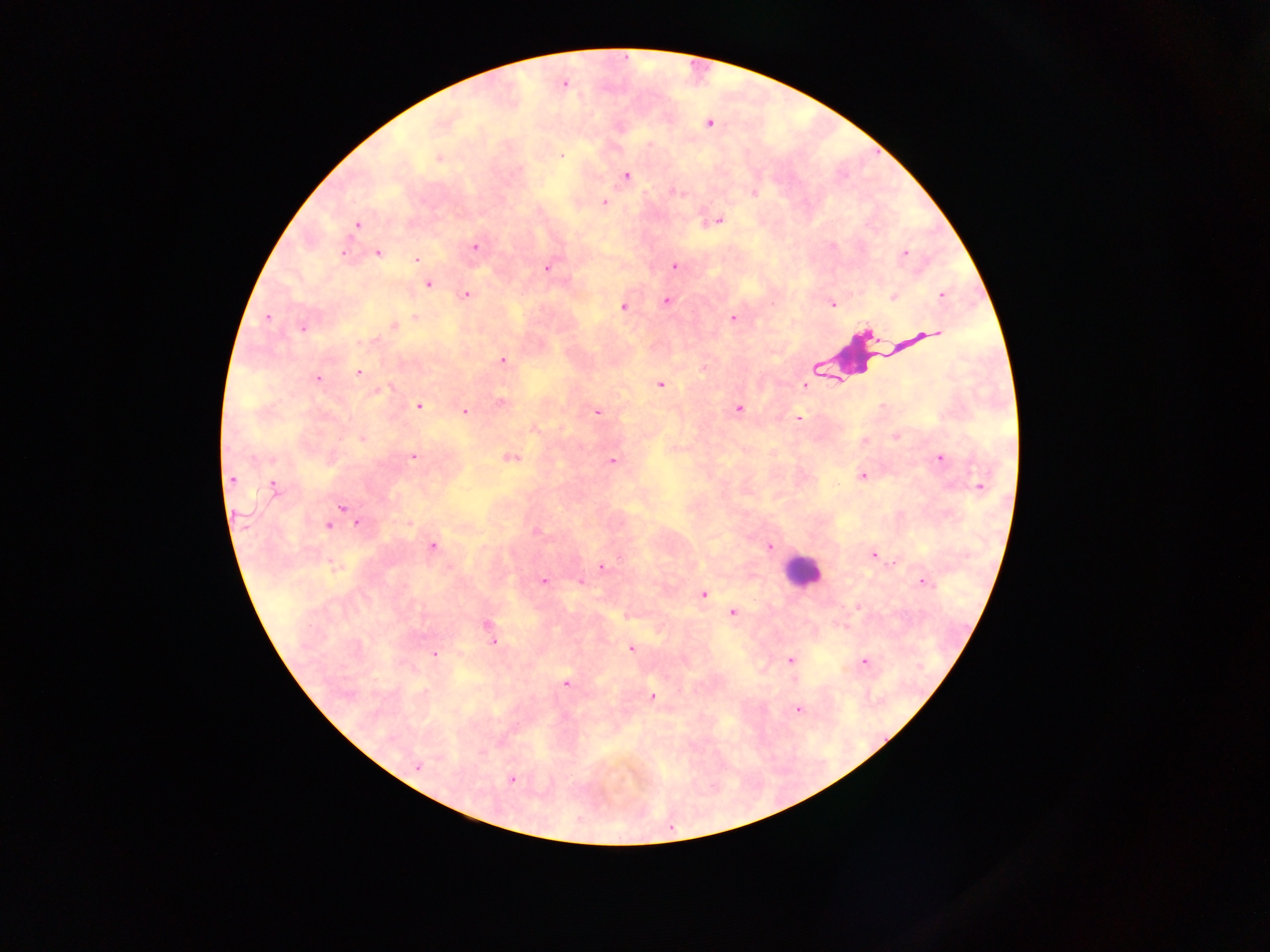

leukocyte locations = approximate centers as {x, y} in pixels: {853, 352}, {802, 576}
country = Ghana
image size = 1270×952 pixels
field of view = single
Plasmodium parasite locations = approximate centers as {x, y} in pixels: {707, 123}, {561, 155}, {439, 158}, {627, 174}, {674, 190}, {754, 193}, {605, 202}, {719, 218}, {357, 224}, {472, 247}, {343, 251}, {905, 252}, {378, 253}, {417, 259}, {674, 264}, {547, 268}, {427, 284}, {465, 295}, {894, 296}, {940, 297}, {667, 301}, {833, 305}, {623, 307}, {413, 314}, {267, 318}, {733, 318}, {393, 326}, {935, 330}, {904, 343}, {899, 345}, {502, 359}, {704, 369}, {358, 373}, {320, 377}, {805, 383}, {660, 386}, {500, 402}, {419, 406}, {739, 408}, {882, 409}, {465, 411}, {598, 412}, {798, 417}, {534, 429}, {895, 436}, {362, 439}, {863, 441}, {414, 455}, {507, 457}, {941, 458}, {613, 460}, {861, 477}, {233, 480}, {273, 486}, {341, 507}, {238, 513}, {408, 523}, {358, 525}, {328, 527}, {537, 530}, {433, 546}, {769, 547}, {875, 554}, {331, 565}, {601, 566}, {543, 581}, {920, 582}, {581, 583}, {703, 594}, {734, 613}, {488, 627}, {493, 641}, {630, 647}, {433, 655}, {788, 660}, {864, 661}, {567, 683}, {653, 696}, {797, 709}, {416, 770}, {512, 780}
capture = mobile-phone photograph through a microscope
preparation = thick blood smear